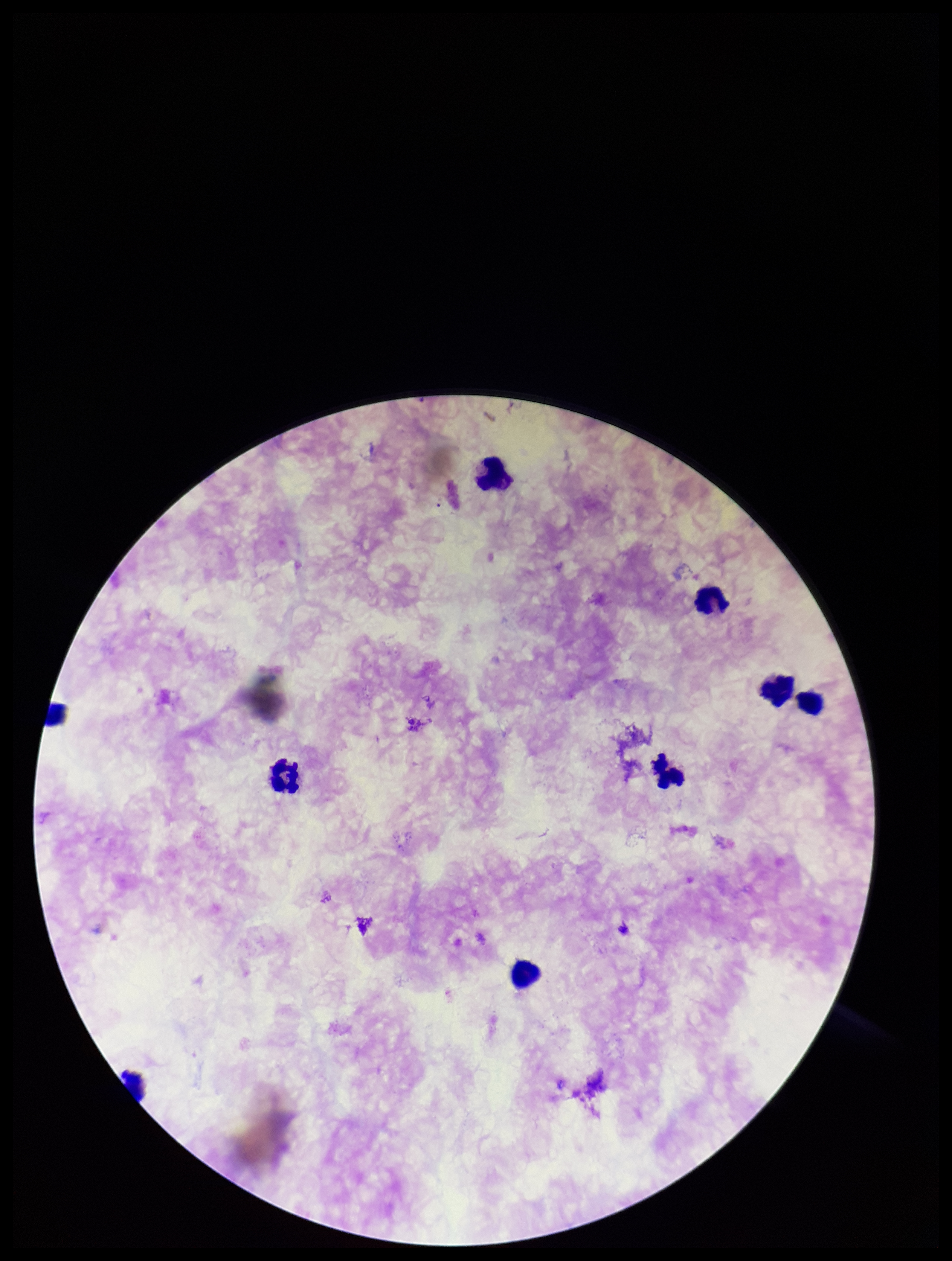
Summary:
  - Plasmodium parasites: none seen
  - Species reported for this patient: Plasmodium falciparum
  - Capture: smartphone photograph through the microscope eyepiece
  - Parasite count: 0
  - Field of view: single
  - Image size: 952×1261 pixels
  - Patient malaria status: infected
  - Leukocyte count: 9
  - Preparation: thick smear
  - Stain: Giemsa